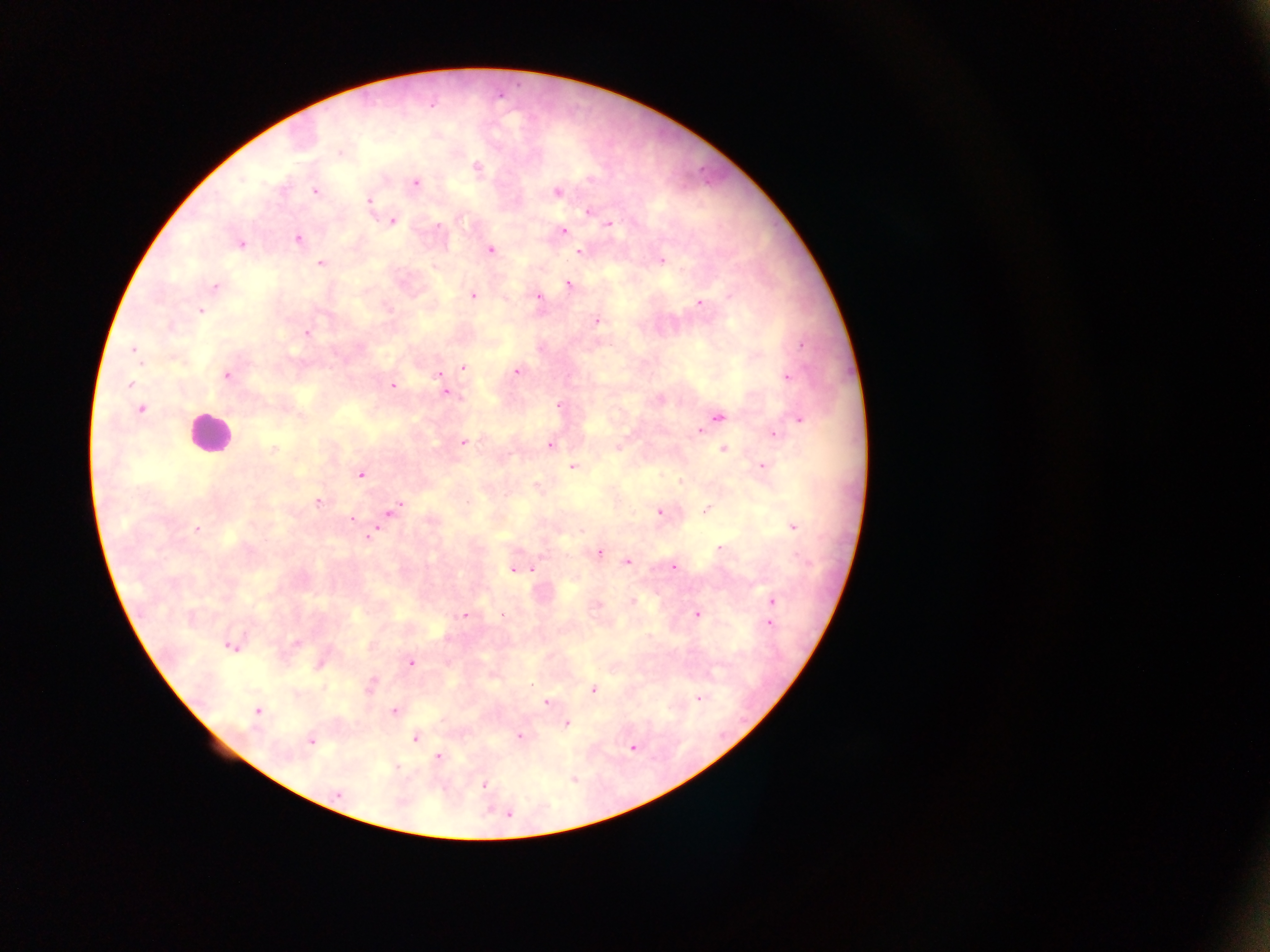
plasmodium_parasite_locations: 'approximate centers as {x, y} in pixels: {339, 153}, {477, 168}, {415, 183}, {314, 191}, {558, 192}, {369, 202}, {588, 210}, {392, 221}, {437, 224}, {609, 225}, {563, 231}, {297, 238}, {242, 245}, {489, 249}, {580, 251}, {660, 260}, {322, 265}, {567, 284}, {214, 287}, {471, 295}, {536, 298}, {701, 303}, {200, 312}, {596, 319}, {305, 331}, {800, 343}, {132, 351}, {138, 357}, {464, 368}, {516, 372}, {227, 376}, {438, 376}, {787, 376}, {130, 382}, {392, 386}, {447, 391}, {462, 395}, {559, 404}, {141, 407}, {720, 417}, {799, 418}, {700, 432}, {774, 433}, {465, 442}, {551, 445}, {723, 449}, {761, 465}, {574, 467}, {359, 474}, {679, 481}, {536, 486}, {318, 501}, {706, 507}, {394, 508}, {659, 511}, {351, 520}, {198, 528}, {791, 528}, {374, 532}, {719, 549}, {598, 552}, {626, 562}, {673, 566}, {532, 568}, {514, 569}, {632, 600}, {771, 600}, {595, 605}, {695, 613}, {501, 614}, {465, 615}, {769, 625}, {295, 643}, {229, 646}, {235, 646}, {408, 662}, {315, 669}, {533, 684}, {323, 687}, {592, 690}, {700, 699}, {546, 703}, {258, 709}, {393, 711}, {568, 724}, {519, 736}, {416, 738}, {310, 741}, {630, 749}, {438, 756}, {575, 780}, {484, 785}, {336, 795}, {510, 815}'
field_of_view: single
capture: mobile-phone photograph through a microscope
preparation: thick blood smear
image_size: 1270×952 pixels
leukocyte_locations: 'approximate centers as {x, y} in pixels: {201, 440}'
country: Ghana